Assess this cell for malaria.
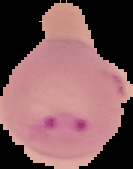
Parasitized.

Summary:
  - Preparation: thin blood smear
  - Image type: cell region segmented out of the field of view; surrounding area masked to black
  - Image size: 133×169 pixels